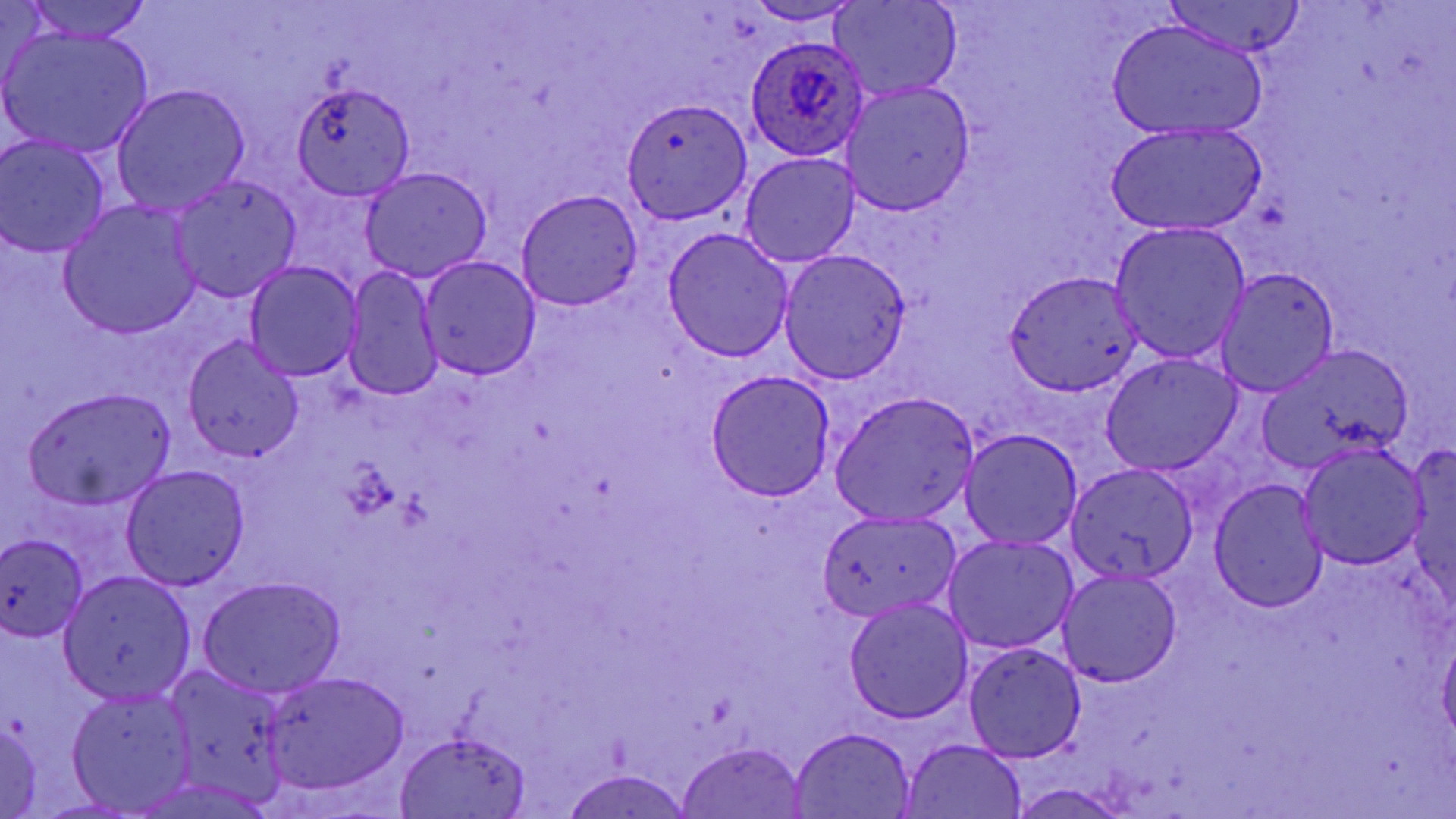
{
  "slide_level_diagnosis": "Plasmodium ovale",
  "stain": "May-Grünwald-Giemsa",
  "field_of_view": "single",
  "magnification": "1000x",
  "plasmodium_ovale_infected_red_blood_cell_locations": "approximate bounding boxes as [x1, y1, x2, y2] in pixels: [745, 34, 872, 160]",
  "preparation": "thin blood smear",
  "uninfected_red_blood_cell_locations": "approximate bounding boxes as [x1, y1, x2, y2] in pixels: [25, 0, 152, 42], [830, 0, 961, 102], [1159, 0, 1305, 60], [744, 1, 863, 25], [1107, 20, 1267, 142], [2, 24, 155, 158], [839, 80, 975, 215], [290, 84, 417, 201], [111, 85, 249, 215], [621, 98, 752, 223], [1106, 124, 1265, 236], [0, 136, 111, 257], [741, 154, 859, 268], [360, 168, 492, 283], [171, 174, 301, 302], [514, 190, 643, 310], [60, 202, 200, 340], [1108, 221, 1251, 364], [663, 228, 793, 362], [778, 250, 911, 383], [417, 256, 542, 381], [243, 262, 363, 380], [1217, 266, 1340, 397], [343, 267, 445, 400], [1002, 270, 1143, 396], [183, 334, 307, 461], [1255, 342, 1412, 476], [1102, 354, 1241, 475], [706, 371, 835, 501], [25, 388, 175, 510], [830, 392, 979, 525], [961, 429, 1084, 548], [1298, 443, 1429, 570], [1066, 463, 1200, 584], [122, 465, 250, 589], [1209, 479, 1328, 614], [816, 510, 962, 622], [0, 534, 88, 641], [942, 536, 1077, 654], [1057, 568, 1182, 687], [61, 571, 195, 703], [197, 577, 345, 700], [844, 598, 974, 723], [1438, 634, 1456, 743], [963, 643, 1087, 762], [163, 664, 294, 797], [263, 670, 409, 793], [67, 692, 196, 812], [0, 722, 45, 818], [790, 727, 917, 818], [393, 729, 530, 819], [900, 738, 1028, 819], [676, 741, 809, 819], [561, 766, 695, 819], [1010, 782, 1135, 819]",
  "modality": "light microscopy",
  "image_size": "1456×819 pixels",
  "platelet_locations": "approximate bounding boxes as [x1, y1, x2, y2] in pixels: [342, 460, 398, 518]"
}